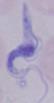 A trypanosome is seen. Micrograph. Captured at 1000x magnification.